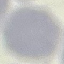

Summary:
  - Result: no malaria parasites detected
  - Stain: Giemsa
  - Image type: cell patch, automatically extracted from a larger field of view and resized to 64 × 64 pixels
  - Preparation: thin smear
  - Capture: smartphone through the microscope eyepiece